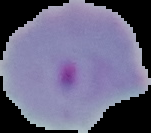
Summary:
  - Image size: 151×133 pixels
  - Image type: segmented cell region on a black background
  - Result: malaria parasites identified
  - Preparation: thin blood film